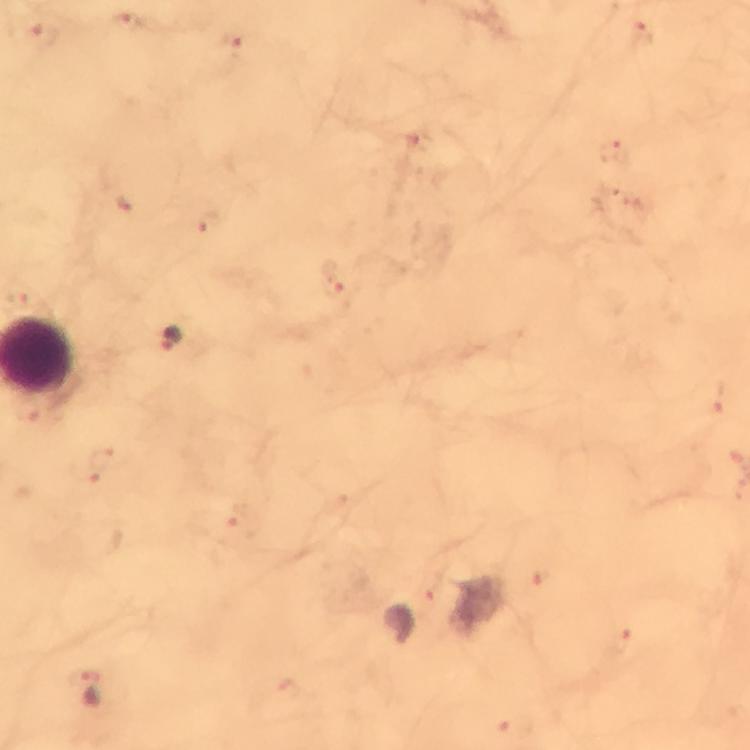

Approximate centers as (x, y) in pixels.
Summary:
  - Malaria parasite locations: (125, 24), (41, 37), (230, 43), (208, 223), (332, 280), (172, 339)
  - Preparation: thick blood film
  - Stain: Giemsa
  - Magnification: 100x
  - Capture: smartphone photograph through a microscope
  - Image size: 750×750 pixels
  - Context: from a malaria diagnostic workup
  - Cropped from: one field of view
  - Immersion oil: applied